Assess the morphology of the red blood cells.
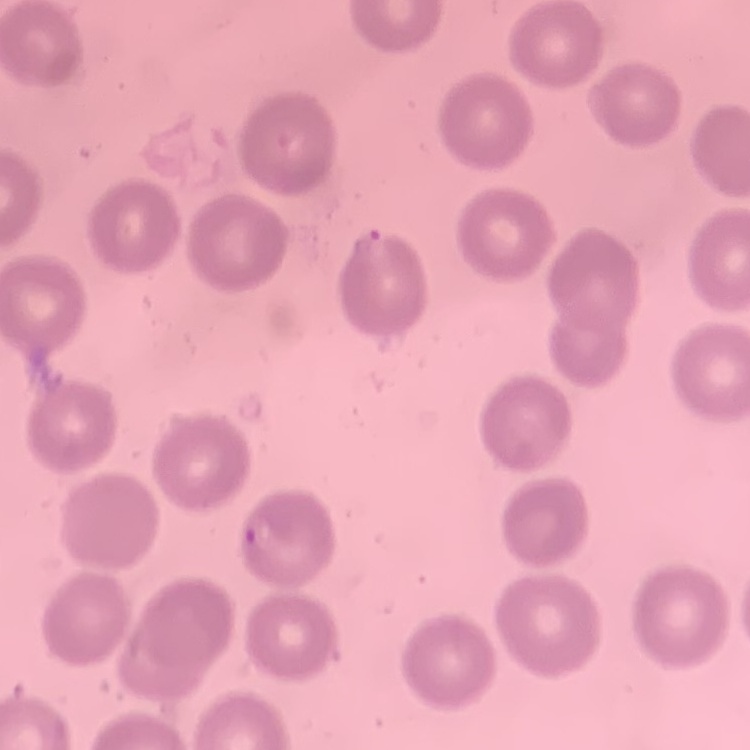
No rouleaux formation.

Stained with either Field's or Giemsa. Square crop of a larger photomicrograph. Thin peripheral smear.